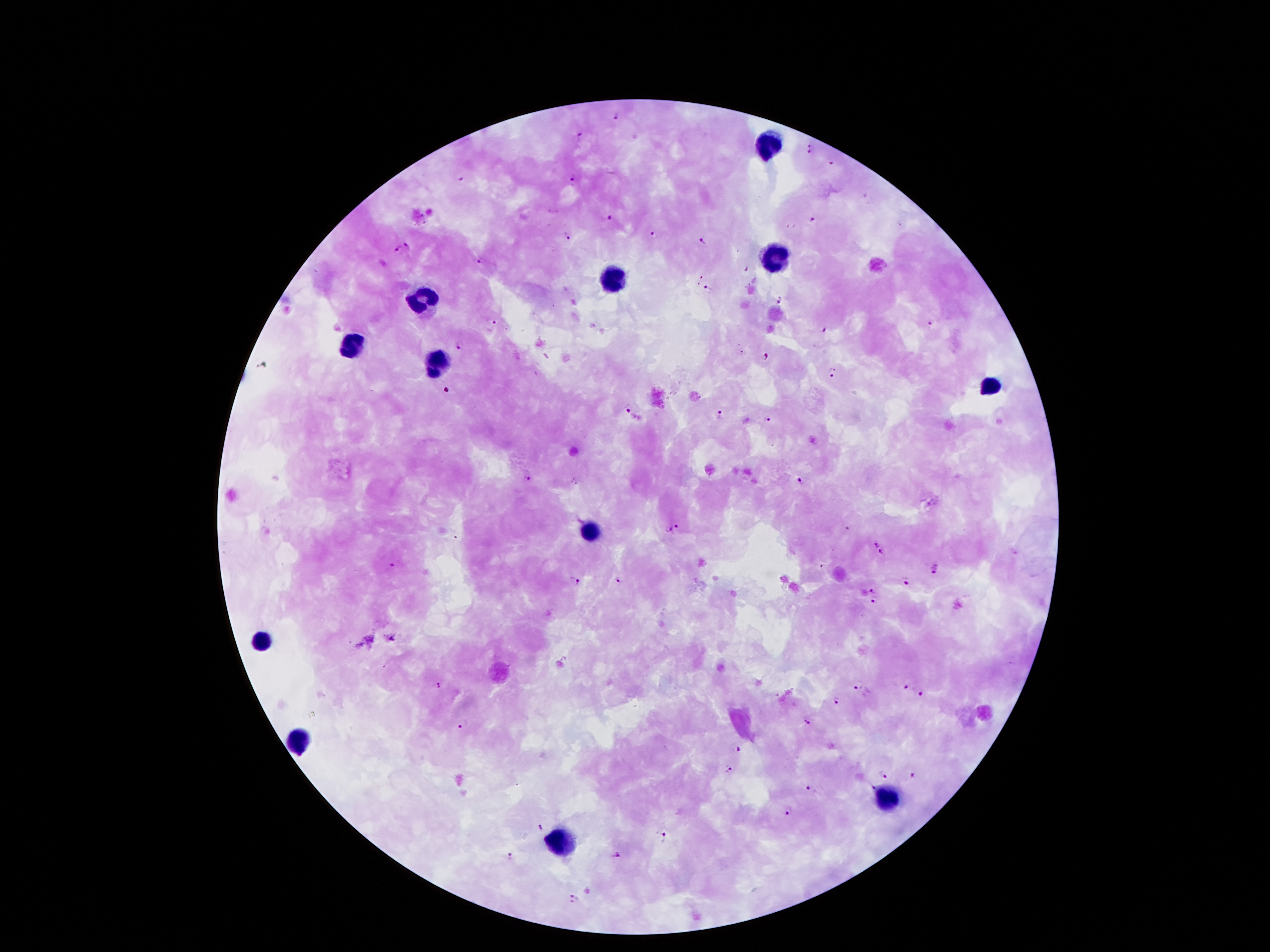

image_size: 1270×952 pixels
plasmodium_parasite_locations: 'approximate object centers, in pixels from the top-left corner: (x=617, y=114), (x=580, y=135), (x=810, y=145), (x=808, y=152), (x=831, y=163), (x=459, y=176), (x=574, y=178), (x=609, y=217), (x=813, y=219), (x=653, y=234), (x=567, y=236), (x=703, y=242), (x=407, y=246), (x=398, y=249), (x=481, y=261), (x=745, y=269), (x=707, y=289), (x=781, y=295), (x=780, y=304), (x=493, y=322), (x=930, y=324), (x=824, y=329), (x=460, y=345), (x=769, y=355), (x=834, y=368), (x=832, y=377), (x=628, y=409), (x=719, y=414), (x=769, y=419), (x=528, y=478), (x=800, y=480), (x=676, y=525), (x=847, y=528), (x=668, y=529), (x=877, y=546), (x=882, y=553), (x=392, y=564), (x=822, y=567), (x=937, y=570), (x=572, y=581), (x=618, y=581), (x=906, y=582), (x=872, y=590), (x=873, y=600), (x=393, y=639), (x=439, y=685), (x=857, y=685), (x=906, y=685), (x=922, y=691), (x=837, y=701), (x=807, y=721), (x=464, y=722), (x=736, y=748), (x=730, y=768), (x=883, y=774), (x=913, y=775), (x=873, y=787), (x=811, y=788), (x=790, y=810), (x=540, y=826), (x=664, y=838), (x=510, y=854), (x=617, y=856), (x=572, y=899)'
capture: smartphone through the microscope eyepiece
leukocyte_locations: 'approximate object centers, in pixels from the top-left corner: (x=768, y=145), (x=776, y=260), (x=612, y=279), (x=425, y=300), (x=354, y=342), (x=438, y=365), (x=988, y=388), (x=591, y=533), (x=266, y=638), (x=299, y=741), (x=887, y=800), (x=560, y=842)'
patient_malaria_status: infected with Plasmodium falciparum
magnification: 100x
stain: Giemsa
field_of_view: one from this slide
preparation: thick blood smear